Describe the morphology of the red blood cells.
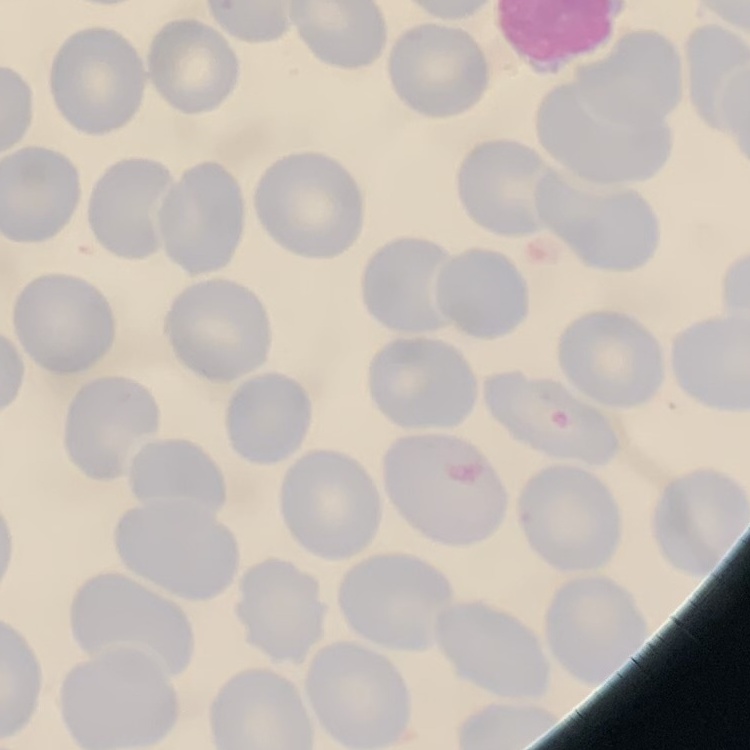

No rouleaux formation.

stain: Field's or Giemsa
preparation: thin blood film
image_type: one tile cut from a larger photomicrograph